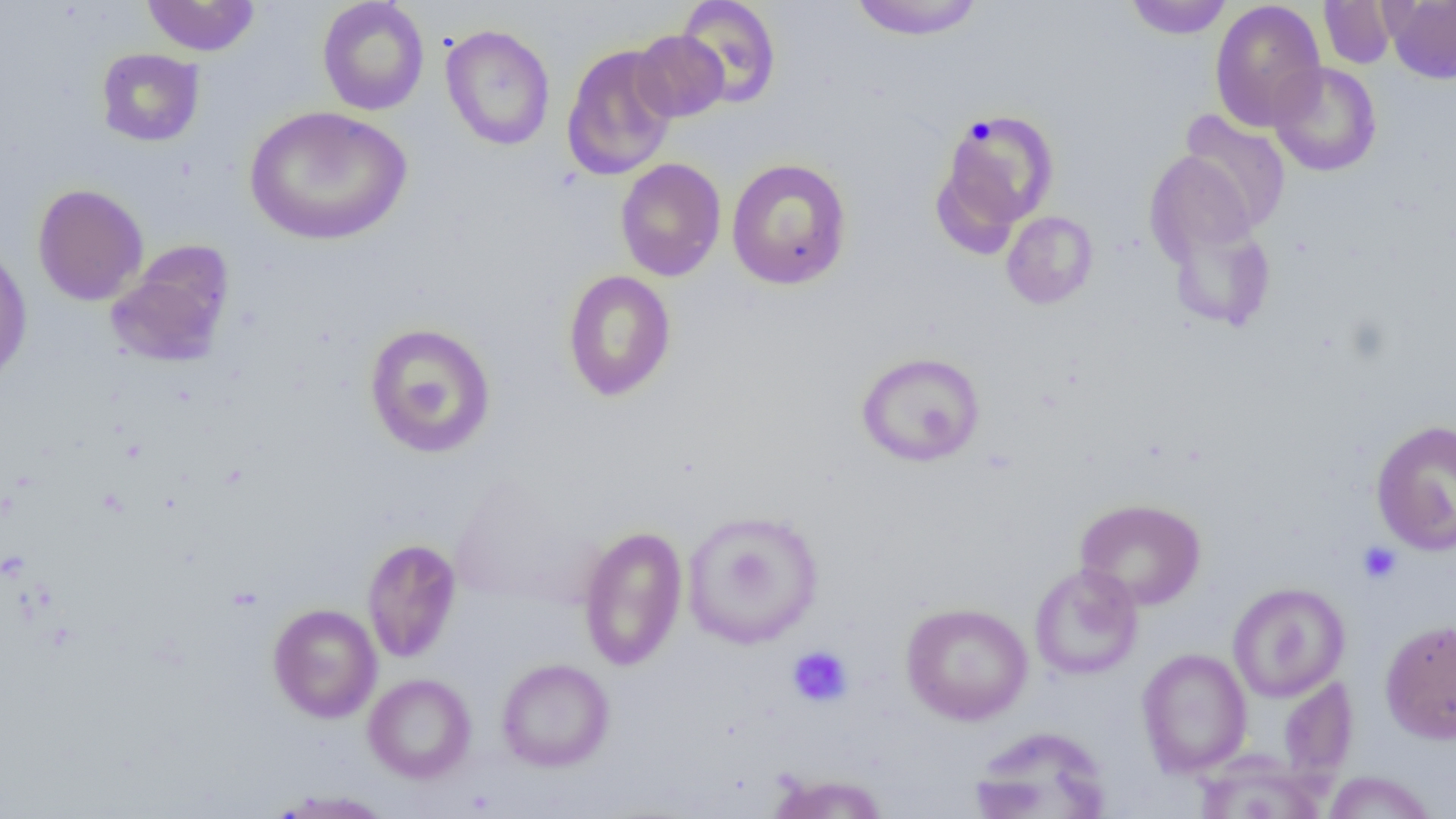
Summary:
  - Coordinate format: approximate bounding boxes as [x1, y1, x2, y2] in pixels
  - Uninfected red blood cell locations: [141, 0, 259, 57], [317, 0, 430, 116], [674, 0, 782, 109], [847, 0, 987, 40], [1124, 0, 1234, 39], [1209, 0, 1326, 132], [1382, 0, 1456, 84], [1318, 1, 1399, 69], [440, 24, 556, 151], [632, 30, 729, 123], [561, 44, 679, 180], [96, 48, 204, 147], [1268, 62, 1382, 177], [244, 105, 412, 246], [933, 108, 1060, 243], [1179, 110, 1291, 232], [1144, 150, 1262, 267], [615, 157, 726, 282], [726, 158, 852, 290], [32, 183, 148, 306], [1002, 211, 1098, 309], [1164, 214, 1276, 332], [107, 241, 235, 368], [0, 243, 32, 386], [561, 269, 677, 402], [363, 322, 496, 458], [855, 351, 986, 467], [1370, 418, 1456, 557], [449, 478, 588, 607], [1075, 498, 1206, 610], [682, 509, 824, 649], [578, 525, 688, 671], [362, 538, 462, 663], [1029, 563, 1143, 680], [1227, 582, 1350, 702], [900, 601, 1033, 725], [267, 603, 382, 723], [1379, 619, 1456, 744], [1136, 648, 1252, 777], [496, 658, 615, 772], [363, 673, 476, 783], [1278, 677, 1358, 784], [968, 726, 1112, 818], [1194, 754, 1326, 819], [1322, 771, 1438, 818], [766, 773, 890, 818], [266, 789, 396, 818]
  - Platelet locations: [967, 115, 998, 146], [1358, 541, 1402, 584], [787, 645, 853, 707]
  - Slide-level diagnosis: negative for blood parasites
  - Preparation: thin blood smear
  - Image size: 1456×819 pixels
  - Field of view: single
  - Modality: optical microscopy
  - Magnification: 1000x